Give the position of every Plasmodium parasite.
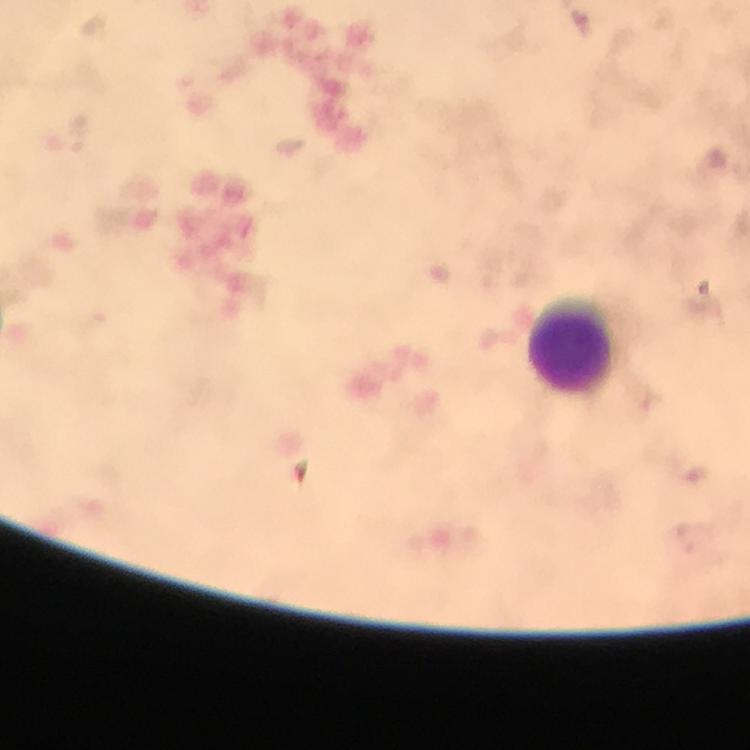

No Plasmodium parasites seen.

Approximate centers as (x, y) in pixels.
Summary:
  - Leukocyte locations: (573, 344)
  - Immersion oil: applied
  - Cropped from: one field of view
  - Capture: smartphone photograph through a microscope
  - Magnification: 100x
  - Stain: Giemsa
  - Image size: 750×750 pixels
  - Preparation: thick blood smear
  - Context: from a malaria diagnostic workup